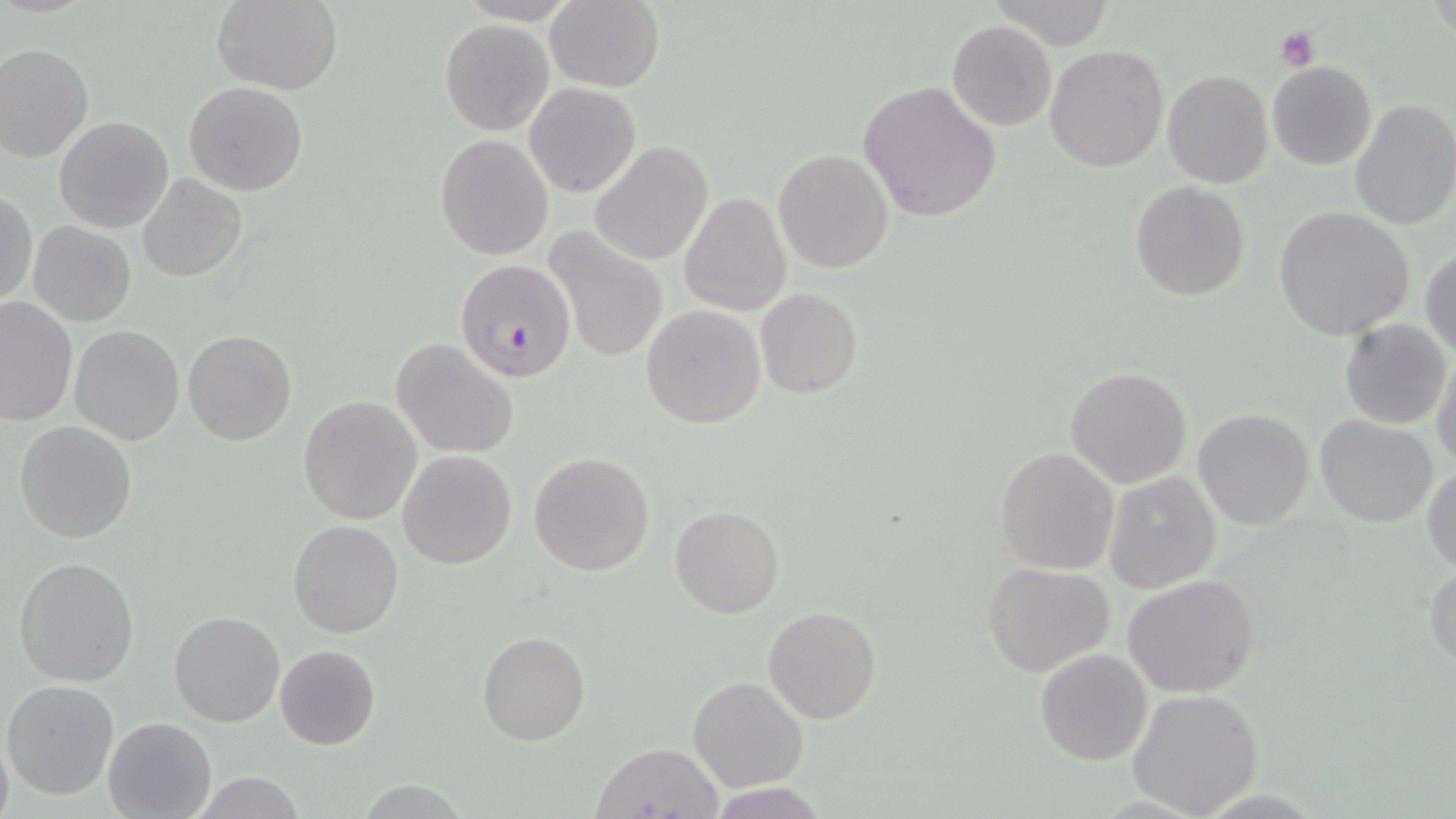

Summary:
  - Coordinate format: approximate bounding boxes as (x1,y1)-(x2,y2) corner pairs in pixels
  - Plasmodium falciparum-infected red blood cell locations: (455,258)-(577,383)
  - Uninfected red blood cell locations: (210,0)-(344,93), (543,1)-(665,91), (439,20)-(553,135), (946,20)-(1058,132), (0,43)-(94,164), (1045,44)-(1168,173), (1266,61)-(1378,171), (1161,70)-(1274,188), (857,80)-(1003,223), (183,82)-(309,197), (524,83)-(641,198), (1349,97)-(1456,230), (53,116)-(175,235), (435,134)-(554,259), (589,142)-(713,265), (772,149)-(894,275), (134,174)-(249,284), (1130,182)-(1250,301), (1,191)-(37,309), (679,193)-(791,316), (1275,207)-(1415,341), (28,222)-(136,327), (542,227)-(668,363), (1420,247)-(1456,360), (755,288)-(863,399), (0,297)-(77,428), (640,305)-(765,429), (1338,317)-(1452,430), (68,325)-(185,445), (182,328)-(298,447), (391,337)-(522,459), (1430,354)-(1456,473), (1064,366)-(1193,489), (297,394)-(422,525), (1193,408)-(1314,530), (1315,414)-(1437,528), (13,419)-(137,543), (993,447)-(1120,575), (397,450)-(518,570), (528,452)-(656,576), (1424,466)-(1456,577), (1103,472)-(1221,594), (669,504)-(784,620), (287,520)-(404,638), (13,556)-(141,687), (1425,562)-(1456,673), (982,563)-(1116,678), (1123,574)-(1260,697), (763,607)-(881,725), (169,611)-(286,728), (477,630)-(590,745), (274,644)-(382,751), (1034,648)-(1154,767), (687,677)-(810,793), (2,679)-(119,800), (1125,687)-(1263,818), (102,716)-(216,819), (0,727)-(14,819), (587,740)-(726,818)
  - Platelet locations: (1275,25)-(1320,72)
  - Slide-level diagnosis: Plasmodium falciparum
  - Field of view: one of a larger specimen
  - Preparation: thin blood smear
  - Image size: 1456×819 pixels
  - Stain: May-Grünwald-Giemsa
  - Modality: optical microscopy
  - Magnification: 1000x